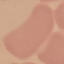

Summary:
  - Result: no malaria parasites seen
  - Image type: cell patch, automatically extracted from a larger field of view and resized to 64 × 64 pixels
  - Stain: Giemsa
  - Capture: smartphone camera at the microscope eyepiece
  - Preparation: thin blood smear